Name the parasite shown.
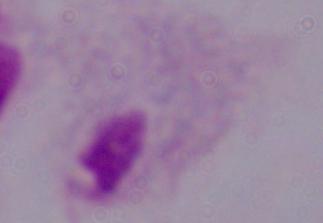
A trichomonad.

Summary:
  - Modality: photomicrograph
  - Magnification: 1000x